Describe the morphology of the red blood cells.
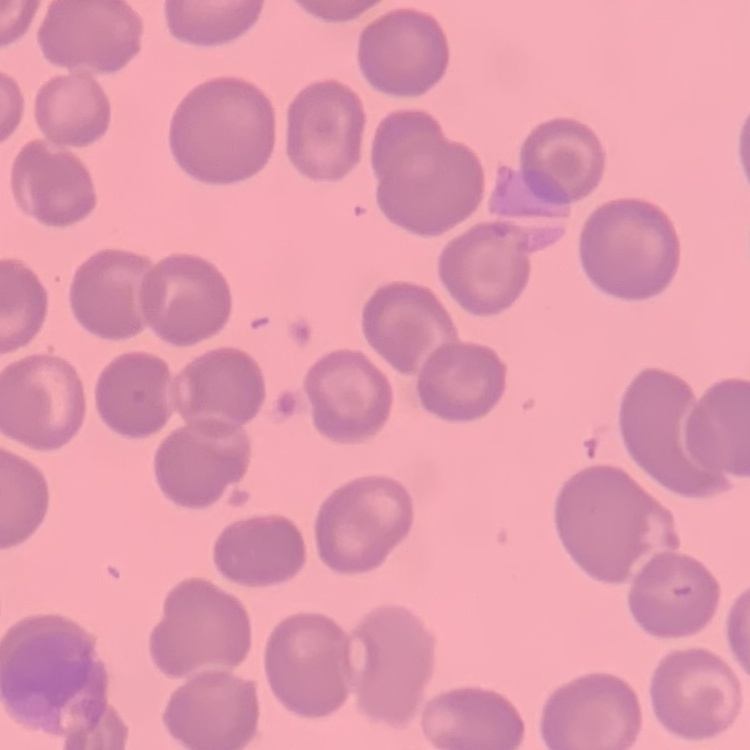

No rouleaux formation.

Summary:
  - Stain: Field's or Giemsa
  - Image type: square crop of a larger photomicrograph
  - Preparation: thin blood film